Report the malaria status of this cell.
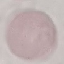
Uninfected.

image_type: cell patch, automatically extracted from a larger field of view and resized to 64 × 64 pixels
capture: smartphone through the microscope eyepiece
preparation: thin blood smear
stain: Giemsa